Name the parasite shown.
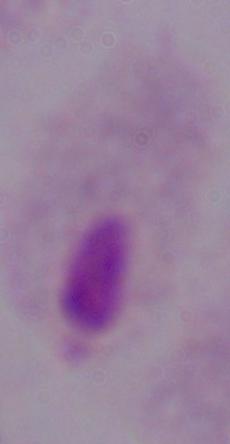

This is a trichomonad.

Summary:
  - Magnification: 1000x
  - Modality: photomicrograph